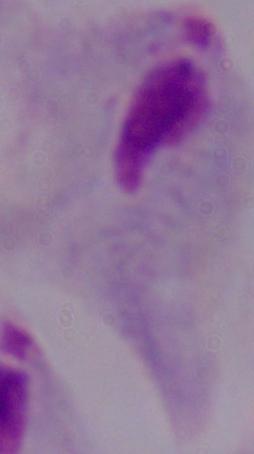

identification = trichomonad
modality = photomicrograph
magnification = 1000x